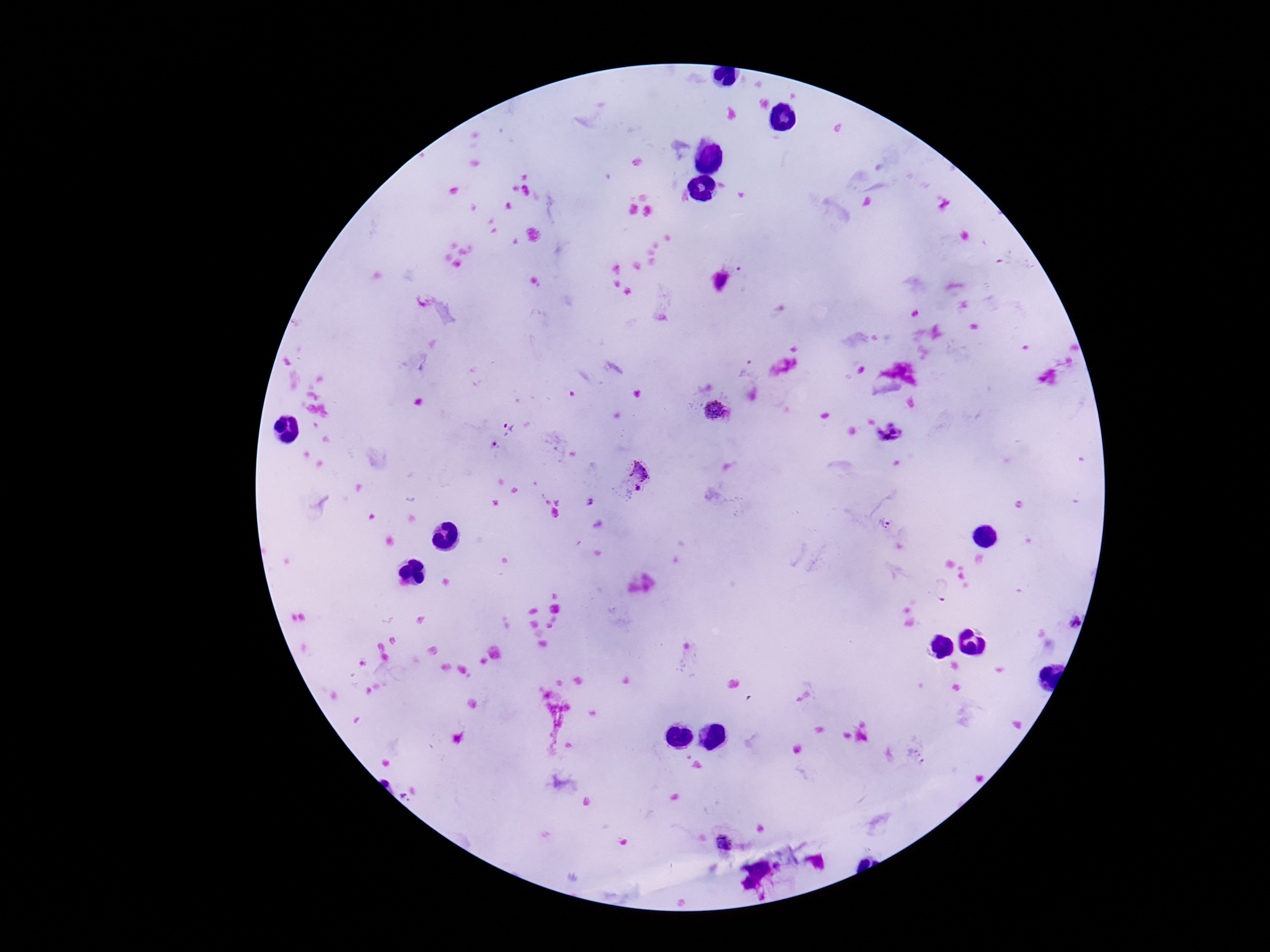
Approximate object centers, in pixels from the top-left corner.
Summary:
  - Plasmodium parasite locations: (x=716, y=413), (x=508, y=428), (x=892, y=432), (x=494, y=446), (x=636, y=472), (x=636, y=491), (x=590, y=502), (x=884, y=524), (x=943, y=589), (x=1075, y=623), (x=727, y=841)
  - Patient malaria status: positive
  - Image size: 1270×952 pixels
  - Magnification: 100x
  - Preparation: thick blood smear
  - Field of view: single
  - Stain: Giemsa
  - Capture: smartphone camera through the microscope eyepiece